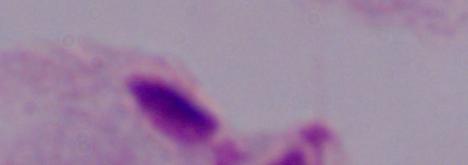
Summary:
  - Magnification: 1000x
  - Identification: trichomonad
  - Modality: photomicrograph